Report the malaria status of this cell.
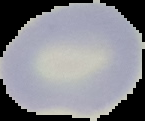
Uninfected.

From a thin blood smear. Image is 145×121 pixels. Cell region segmented out of the field of view; the surrounding area is masked to black.